Assess this cell for malaria.
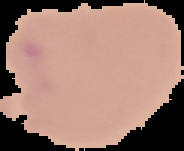

Parasitized.

Cell region segmented out of the field of view; the surrounding area is masked to black. Image is 184×151 pixels. From a thin blood smear.